State the blood parasite species.
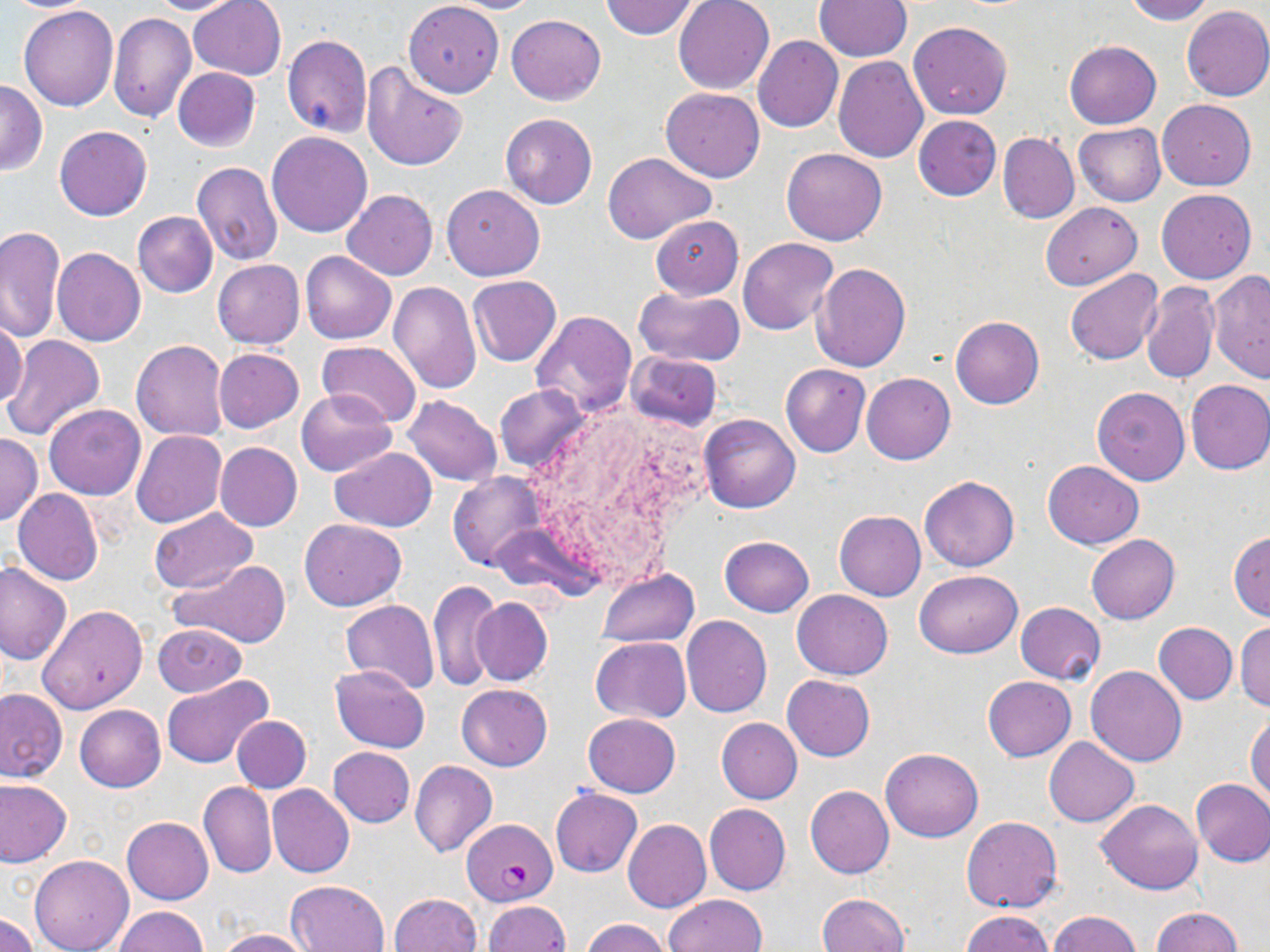

Plasmodium falciparum.

{
  "stain": "May-Grünwald-Giemsa",
  "image_size": "1270×952 pixels",
  "uninfected_red_blood_cell_locations": "approximate bounding boxes as named x1/y1/x2/y2 corners in pixels: (x1=2, y1=0, x2=99, y2=12), (x1=144, y1=0, x2=250, y2=15), (x1=187, y1=0, x2=286, y2=79), (x1=444, y1=0, x2=542, y2=13), (x1=599, y1=0, x2=700, y2=40), (x1=673, y1=0, x2=774, y2=94), (x1=815, y1=0, x2=910, y2=61), (x1=1121, y1=0, x2=1214, y2=24), (x1=404, y1=1, x2=504, y2=96), (x1=19, y1=4, x2=119, y2=111), (x1=1182, y1=5, x2=1270, y2=101), (x1=107, y1=13, x2=197, y2=124), (x1=505, y1=14, x2=606, y2=105), (x1=908, y1=20, x2=1012, y2=120), (x1=281, y1=35, x2=372, y2=137), (x1=754, y1=36, x2=843, y2=132), (x1=1064, y1=41, x2=1161, y2=129), (x1=833, y1=56, x2=929, y2=161), (x1=362, y1=63, x2=468, y2=171), (x1=173, y1=67, x2=260, y2=152), (x1=0, y1=79, x2=47, y2=175), (x1=660, y1=87, x2=765, y2=182), (x1=1158, y1=99, x2=1255, y2=190), (x1=501, y1=113, x2=597, y2=210), (x1=913, y1=115, x2=1001, y2=200), (x1=1073, y1=122, x2=1166, y2=206), (x1=54, y1=125, x2=151, y2=221), (x1=266, y1=130, x2=374, y2=237), (x1=998, y1=132, x2=1079, y2=225), (x1=781, y1=147, x2=887, y2=245), (x1=602, y1=152, x2=717, y2=243), (x1=192, y1=161, x2=282, y2=266), (x1=441, y1=185, x2=545, y2=280), (x1=1157, y1=188, x2=1256, y2=284), (x1=341, y1=190, x2=438, y2=279), (x1=1041, y1=202, x2=1141, y2=290), (x1=132, y1=211, x2=218, y2=297), (x1=652, y1=216, x2=743, y2=298), (x1=0, y1=225, x2=66, y2=343), (x1=738, y1=237, x2=838, y2=336), (x1=52, y1=248, x2=145, y2=346), (x1=301, y1=251, x2=395, y2=344), (x1=212, y1=260, x2=305, y2=349), (x1=812, y1=262, x2=911, y2=371), (x1=1064, y1=269, x2=1163, y2=365), (x1=1208, y1=270, x2=1270, y2=385), (x1=468, y1=275, x2=561, y2=367), (x1=1140, y1=281, x2=1218, y2=383), (x1=388, y1=282, x2=482, y2=394), (x1=633, y1=287, x2=745, y2=367), (x1=529, y1=309, x2=637, y2=415), (x1=0, y1=315, x2=26, y2=410), (x1=950, y1=316, x2=1045, y2=409), (x1=3, y1=335, x2=106, y2=441), (x1=131, y1=340, x2=229, y2=441), (x1=316, y1=340, x2=423, y2=426), (x1=213, y1=348, x2=303, y2=434), (x1=627, y1=351, x2=723, y2=430), (x1=780, y1=363, x2=871, y2=457), (x1=861, y1=372, x2=955, y2=464), (x1=1184, y1=379, x2=1270, y2=475), (x1=495, y1=384, x2=590, y2=474), (x1=1091, y1=387, x2=1190, y2=485), (x1=295, y1=388, x2=396, y2=476), (x1=403, y1=395, x2=503, y2=485), (x1=44, y1=404, x2=146, y2=500), (x1=699, y1=412, x2=801, y2=514), (x1=132, y1=430, x2=227, y2=530), (x1=0, y1=433, x2=43, y2=528), (x1=214, y1=442, x2=302, y2=531), (x1=331, y1=446, x2=437, y2=532), (x1=1043, y1=461, x2=1143, y2=549), (x1=447, y1=471, x2=548, y2=570), (x1=920, y1=475, x2=1018, y2=572), (x1=13, y1=488, x2=103, y2=585), (x1=148, y1=508, x2=255, y2=594), (x1=833, y1=510, x2=926, y2=602), (x1=298, y1=518, x2=408, y2=611), (x1=1228, y1=531, x2=1270, y2=621), (x1=1086, y1=534, x2=1180, y2=623), (x1=719, y1=535, x2=814, y2=616), (x1=170, y1=560, x2=291, y2=649), (x1=0, y1=564, x2=71, y2=665), (x1=597, y1=568, x2=699, y2=647), (x1=915, y1=570, x2=1023, y2=657), (x1=429, y1=581, x2=499, y2=690), (x1=792, y1=590, x2=893, y2=679), (x1=471, y1=597, x2=552, y2=686), (x1=339, y1=598, x2=440, y2=693), (x1=1015, y1=603, x2=1105, y2=684), (x1=37, y1=604, x2=147, y2=715), (x1=681, y1=615, x2=772, y2=717), (x1=1234, y1=621, x2=1270, y2=712), (x1=1153, y1=622, x2=1238, y2=704), (x1=153, y1=624, x2=246, y2=698), (x1=591, y1=637, x2=690, y2=722), (x1=331, y1=664, x2=430, y2=752), (x1=1086, y1=666, x2=1187, y2=767), (x1=782, y1=675, x2=875, y2=762), (x1=983, y1=675, x2=1076, y2=761), (x1=161, y1=676, x2=272, y2=770), (x1=457, y1=684, x2=553, y2=770), (x1=0, y1=688, x2=67, y2=782), (x1=75, y1=705, x2=166, y2=792), (x1=1247, y1=713, x2=1270, y2=803), (x1=583, y1=714, x2=679, y2=797), (x1=233, y1=716, x2=310, y2=793), (x1=716, y1=717, x2=802, y2=803), (x1=1044, y1=738, x2=1139, y2=826), (x1=327, y1=746, x2=415, y2=827), (x1=880, y1=747, x2=983, y2=842), (x1=410, y1=761, x2=497, y2=858), (x1=0, y1=779, x2=72, y2=866), (x1=1191, y1=779, x2=1270, y2=866), (x1=198, y1=781, x2=277, y2=878), (x1=267, y1=784, x2=354, y2=877), (x1=805, y1=785, x2=894, y2=878), (x1=550, y1=786, x2=642, y2=878), (x1=1096, y1=799, x2=1201, y2=894), (x1=704, y1=804, x2=792, y2=896), (x1=961, y1=815, x2=1063, y2=912), (x1=122, y1=817, x2=214, y2=905), (x1=624, y1=820, x2=712, y2=913), (x1=29, y1=854, x2=134, y2=952), (x1=286, y1=880, x2=390, y2=952), (x1=389, y1=893, x2=482, y2=952), (x1=816, y1=893, x2=910, y2=952), (x1=662, y1=894, x2=767, y2=952), (x1=483, y1=901, x2=570, y2=952), (x1=114, y1=906, x2=209, y2=952), (x1=1154, y1=907, x2=1243, y2=952), (x1=960, y1=910, x2=1056, y2=952), (x1=1048, y1=910, x2=1142, y2=952), (x1=0, y1=913, x2=38, y2=952), (x1=581, y1=918, x2=674, y2=952), (x1=213, y1=928, x2=313, y2=951)",
  "field_of_view": "one of a larger specimen",
  "magnification": "1000x",
  "modality": "optical microscopy",
  "preparation": "thin blood film",
  "plasmodium_falciparum_infected_red_blood_cell_locations": "approximate bounding boxes as named x1/y1/x2/y2 corners in pixels: (x1=462, y1=819, x2=557, y2=906)"
}